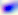

Summary:
  - Magnification: 400x
  - Identification: Toxoplasma gondii
  - Modality: micrograph